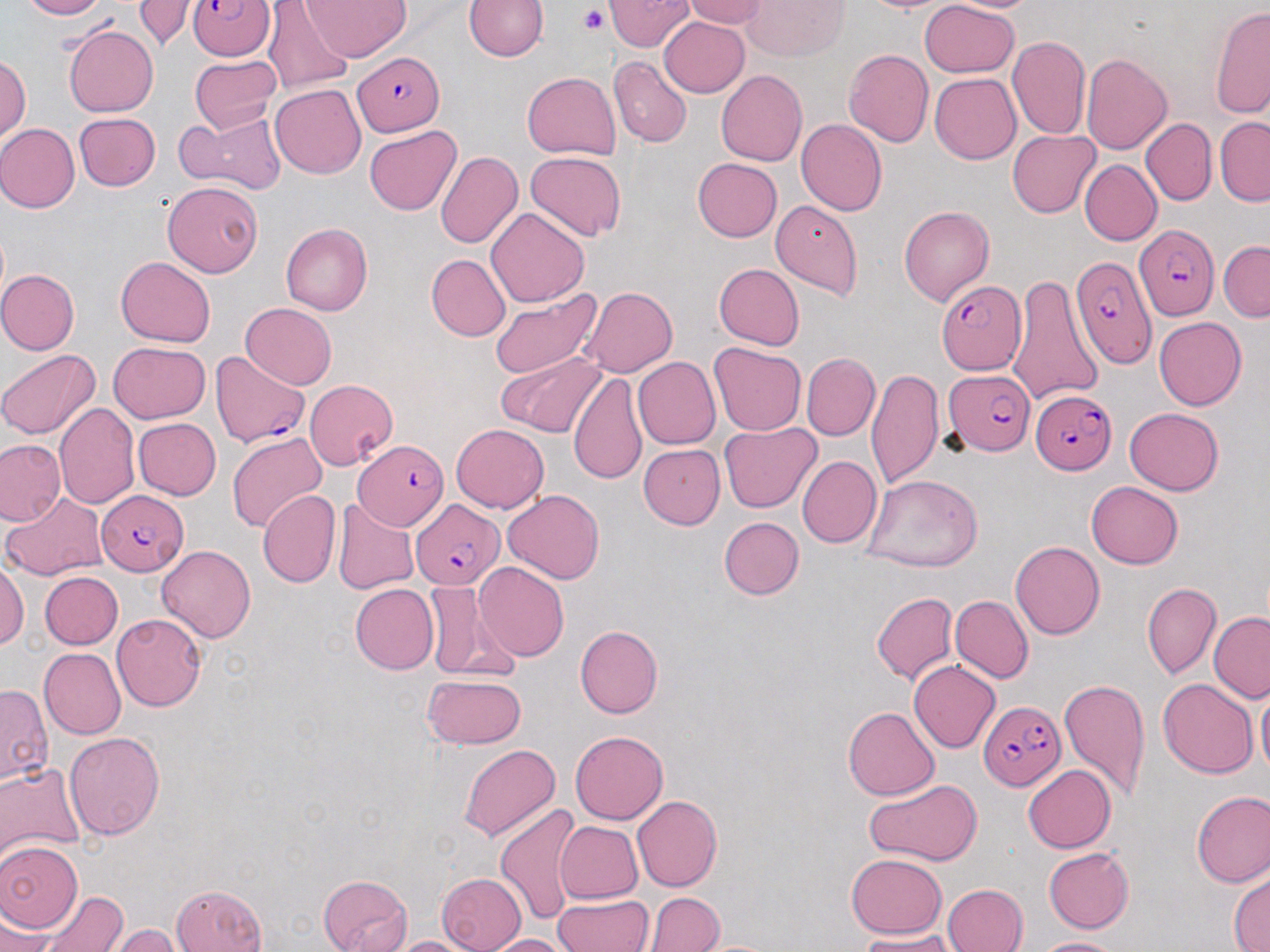

Plasmodium falciparum-infected red blood cell locations = approximate bounding boxes as (x1, y1, x2, y2) in pixels: (189, 0, 276, 61), (352, 53, 446, 134), (1136, 225, 1220, 320), (1072, 258, 1153, 370), (935, 280, 1024, 375), (210, 349, 309, 450), (942, 364, 1033, 455), (1028, 387, 1117, 473), (355, 441, 447, 531), (95, 491, 187, 573), (413, 499, 503, 587), (978, 700, 1065, 793)
slide-level diagnosis = Plasmodium falciparum
magnification = 1000x
image size = 1270×952 pixels
field of view = single
stain = May-Grünwald-Giemsa
modality = light microscopy
uninfected red blood cell locations = approximate bounding boxes as (x1, y1, x2, y2) in pixels: (16, 0, 106, 20), (136, 0, 188, 50), (304, 0, 412, 60), (609, 0, 694, 52), (680, 0, 769, 28), (746, 0, 850, 60), (860, 0, 956, 16), (918, 1, 1020, 78), (464, 2, 547, 62), (266, 4, 355, 90), (1212, 6, 1270, 116), (658, 15, 750, 97), (65, 24, 161, 116), (1008, 35, 1089, 140), (842, 48, 936, 148), (1082, 52, 1173, 155), (0, 53, 29, 147), (190, 54, 282, 133), (612, 57, 691, 145), (716, 69, 811, 167), (521, 72, 621, 160), (929, 73, 1021, 164), (270, 83, 369, 177), (175, 109, 286, 193), (73, 112, 161, 191), (1215, 117, 1270, 203), (797, 118, 887, 215), (1143, 120, 1214, 205), (0, 122, 79, 212), (364, 125, 462, 215), (1008, 129, 1099, 215), (436, 151, 521, 249), (525, 151, 629, 242), (691, 157, 782, 242), (1079, 160, 1160, 246), (164, 182, 263, 278), (771, 199, 862, 298), (898, 202, 994, 302), (487, 206, 589, 306), (280, 223, 371, 315), (1218, 243, 1270, 320), (425, 254, 511, 342), (116, 255, 214, 344), (714, 264, 803, 348), (0, 270, 79, 354), (1006, 270, 1102, 407), (581, 287, 677, 377), (488, 288, 602, 380), (239, 303, 338, 389), (1153, 314, 1246, 407), (709, 342, 806, 435), (107, 343, 211, 424), (0, 348, 102, 442), (497, 352, 608, 438), (802, 353, 878, 439), (631, 358, 720, 449), (867, 368, 944, 489), (569, 371, 646, 483), (303, 379, 398, 469), (56, 402, 138, 508), (1124, 406, 1223, 497), (133, 419, 220, 500), (719, 422, 821, 513), (452, 423, 549, 512), (226, 429, 329, 531), (2, 440, 65, 526), (636, 444, 726, 528), (796, 456, 880, 549), (863, 473, 982, 569), (1087, 479, 1183, 566), (2, 488, 106, 581), (258, 490, 340, 587), (503, 490, 605, 584), (332, 497, 419, 596), (720, 517, 803, 599), (1009, 541, 1103, 640), (158, 543, 258, 641), (0, 562, 28, 653), (474, 563, 569, 661), (40, 571, 122, 648), (425, 581, 499, 678), (1141, 582, 1222, 679), (349, 584, 438, 674), (872, 590, 959, 685), (951, 594, 1033, 681), (1210, 611, 1270, 702), (112, 614, 206, 711), (576, 623, 664, 718), (40, 648, 125, 740), (911, 659, 1003, 753), (421, 673, 528, 748), (1156, 677, 1257, 778), (1057, 678, 1151, 800), (1, 681, 53, 792), (1254, 687, 1269, 777), (842, 706, 939, 801), (66, 730, 164, 840), (570, 731, 668, 823), (459, 743, 559, 844), (0, 761, 85, 869), (1024, 762, 1116, 850), (863, 778, 983, 866), (1192, 790, 1270, 888), (631, 795, 720, 889), (494, 803, 581, 924), (553, 819, 643, 904), (1, 838, 82, 933), (1042, 845, 1135, 934), (845, 854, 947, 938), (435, 872, 527, 952), (1228, 872, 1269, 952), (318, 874, 414, 952), (944, 882, 1028, 951), (167, 886, 269, 952), (37, 887, 130, 952), (553, 892, 656, 952), (649, 892, 725, 952), (1, 912, 53, 952), (114, 925, 182, 951), (850, 930, 956, 949), (387, 933, 475, 952), (485, 933, 576, 951), (1034, 934, 1123, 951)
platelet locations = approximate bounding boxes as (x1, y1, x2, y2) in pixels: (577, 5, 609, 34)
preparation = thin blood film